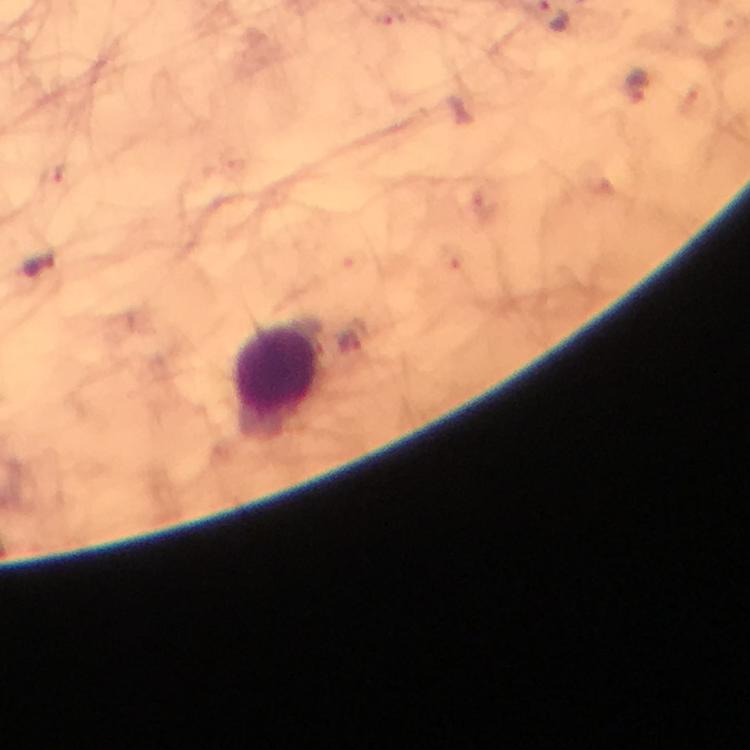

Approximate centers as [x, y] in pixels. Leukocyte locations: [275, 375]. Plasmodium parasite locations: [639, 88], [39, 266]. Giemsa stain. Image is 750×750 pixels. At 100x magnification. Immersion oil applied. Photographed with a smartphone mounted on the microscope. From a diagnostic examination for malaria. Thick blood film. A crop from one field of view.